Identify the parasite.
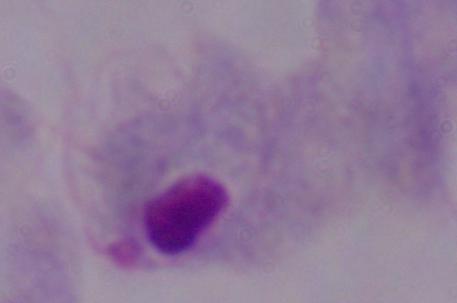

This is a trichomonad.

Summary:
  - Magnification: 1000x
  - Modality: micrograph